Describe the morphology of the red blood cells.
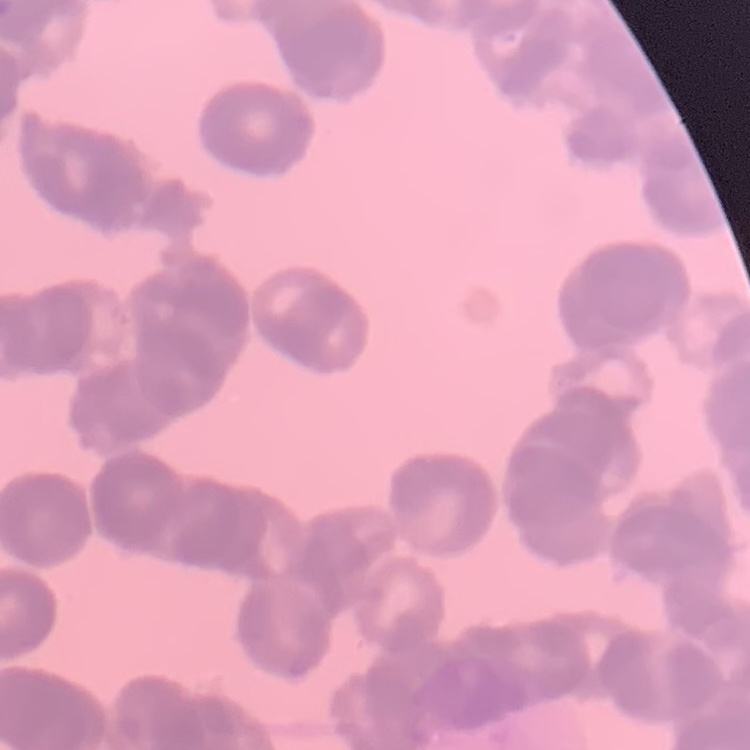
They show rouleaux formation.

stain = Field's or Giemsa
image type = square crop of a larger photomicrograph
preparation = thin blood film